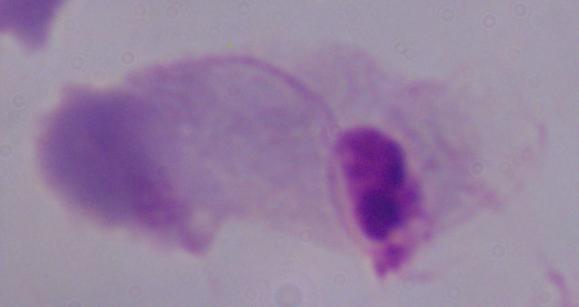
Micrograph. Captured at 1000x magnification. A trichomonad is shown.